Find the cells and give the type of each one.
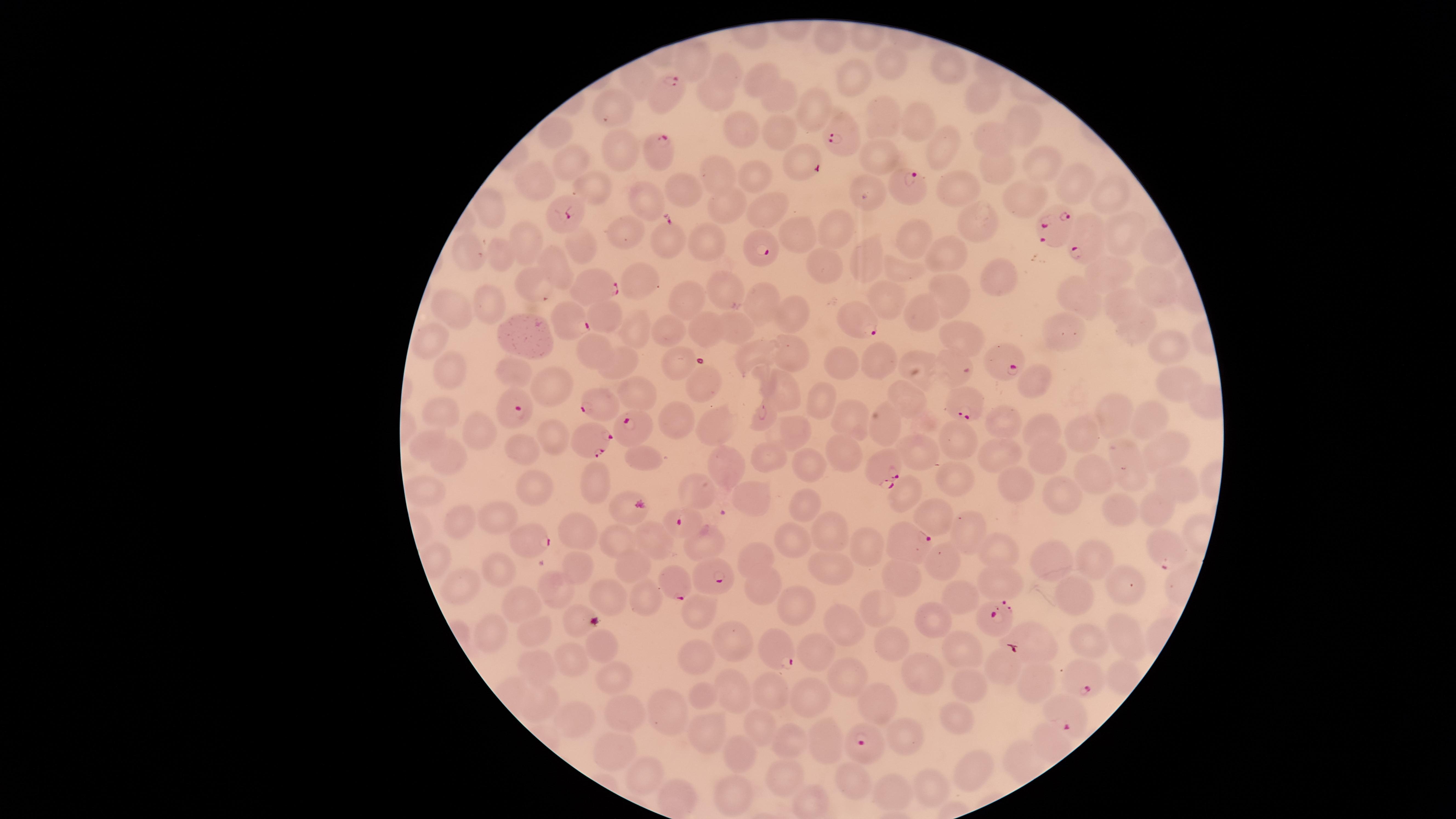

Approximate marker points as {x, y} in pixels.
Parasitized red blood cells: {666, 93}, {843, 132}, {657, 154}, {908, 189}, {577, 208}, {1052, 233}, {764, 241}, {1085, 243}, {597, 283}, {560, 316}, {851, 320}, {1003, 357}, {602, 401}, {509, 403}, {971, 404}, {641, 426}, {589, 434}, {882, 464}, {688, 516}, {524, 534}, {910, 544}, {1162, 547}, {702, 571}, {676, 579}, {988, 621}, {1024, 639}, {772, 645}, {1087, 680}, {1063, 712}, {868, 738}.
Uninfected red blood cells: {829, 38}, {698, 57}, {899, 63}, {947, 63}, {728, 70}, {851, 75}, {768, 80}, {981, 94}, {719, 98}, {616, 101}, {786, 102}, {816, 109}, {886, 117}, {920, 119}, {1023, 123}, {743, 128}, {780, 129}, {553, 135}, {990, 136}, {942, 145}, {880, 148}, {619, 149}, {796, 157}, {1038, 159}, {577, 164}, {995, 167}, {718, 171}, {758, 176}, {537, 180}, {1070, 181}, {863, 182}, {594, 184}, {685, 187}, {958, 187}, {1107, 193}, {1026, 198}, {643, 203}, {725, 204}, {758, 206}, {497, 215}, {979, 216}, {1123, 224}, {797, 227}, {831, 227}, {630, 233}, {706, 237}, {914, 237}, {666, 238}, {525, 243}, {580, 243}, {955, 246}, {470, 254}, {496, 254}, {869, 257}, {821, 264}, {1106, 265}, {553, 266}, {901, 268}, {1161, 279}, {643, 280}, {999, 280}, {538, 282}, {726, 284}, {946, 293}, {893, 294}, {1078, 294}, {692, 296}, {491, 303}, {764, 303}, {1120, 305}, {921, 310}, {455, 311}, {792, 316}, {735, 320}, {1135, 327}, {634, 329}, {703, 329}, {667, 331}, {961, 331}, {1063, 333}, {528, 335}, {428, 339}, {592, 342}, {1167, 348}, {788, 349}, {749, 351}, {918, 356}, {882, 357}, {841, 358}, {625, 362}, {681, 364}, {949, 364}, {449, 367}, {519, 374}, {703, 380}, {1175, 380}, {1033, 381}, {554, 387}, {784, 393}, {816, 395}, {645, 396}, {906, 399}, {446, 412}, {1116, 413}, {765, 415}, {1149, 416}, {847, 417}, {674, 418}, {999, 421}, {882, 423}, {717, 425}, {793, 430}, {1084, 430}, {487, 431}, {1048, 433}, {557, 434}, {963, 435}, {423, 443}, {529, 445}, {1169, 446}, {843, 450}, {998, 451}, {927, 452}, {1055, 452}, {772, 455}, {648, 456}, {451, 457}, {726, 458}, {1133, 463}, {810, 464}, {1095, 470}, {598, 479}, {961, 480}, {1174, 480}, {1015, 481}, {539, 487}, {701, 487}, {907, 488}, {427, 490}, {755, 494}, {1068, 497}, {807, 500}, {621, 505}, {1162, 508}, {1128, 511}, {929, 513}, {499, 514}, {459, 522}, {827, 525}, {582, 531}, {653, 537}, {619, 538}, {791, 538}, {966, 538}, {704, 542}, {861, 544}, {1000, 552}, {754, 554}, {1051, 557}, {1095, 557}, {951, 558}, {634, 566}, {503, 567}, {580, 569}, {836, 569}, {910, 576}, {999, 581}, {1122, 582}, {468, 586}, {763, 586}, {556, 588}, {610, 595}, {964, 597}, {1073, 599}, {650, 602}, {799, 603}, {517, 604}, {697, 607}, {881, 609}, {933, 623}, {853, 624}, {530, 629}, {491, 631}, {1125, 633}, {891, 641}, {739, 642}, {1088, 642}, {602, 645}, {964, 650}, {816, 653}, {574, 658}, {699, 658}, {531, 661}, {1000, 669}, {609, 672}, {920, 672}, {849, 679}, {970, 682}, {1034, 682}, {733, 685}, {772, 689}, {702, 692}, {813, 697}, {540, 701}, {880, 701}, {678, 705}, {624, 713}, {572, 718}, {962, 719}, {761, 722}, {712, 731}, {907, 736}, {786, 738}, {825, 742}, {609, 748}, {741, 756}, {977, 768}, {848, 775}, {648, 776}, {784, 777}, {933, 786}, {891, 791}, {734, 792}, {676, 796}.
No white blood cells identified.

field of view = single
capture = smartphone photograph through the microscope eyepiece
preparation = thin blood smear
species = Plasmodium falciparum
image size = 1456×819 pixels
visible region = circular
stain = Giemsa